Assess the morphology of the red blood cells.
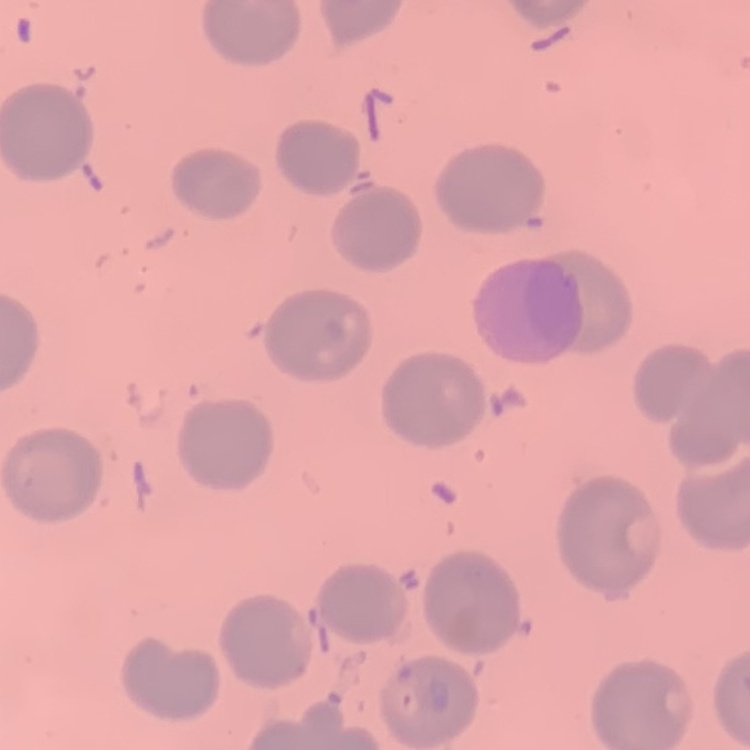
No rouleaux formation.

{
  "stain": "Field's or Giemsa",
  "image_type": "square crop of a larger photomicrograph",
  "preparation": "thin blood smear"
}